Classify this cell by malaria status.
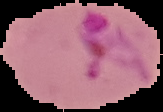
It is parasitized.

{
  "image_size": "163×112 pixels",
  "preparation": "thin blood film",
  "image_type": "segmented cell region with the area outside set to black"
}